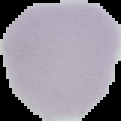
Result: negative for malaria parasites. Image is 121×121 pixels. From a thin blood film. Cell region segmented out of the field of view; the surrounding area is masked to black.